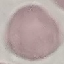

Malaria status: uninfected. Thin blood smear. Giemsa stain. Automatically extracted cell patch, resized to 64 × 64 pixels. Acquired by smartphone through the microscope eyepiece.